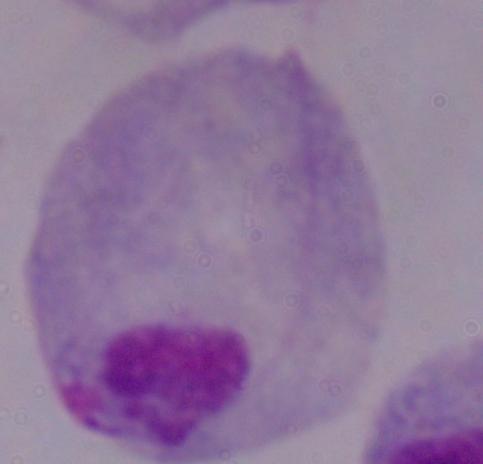

Summary:
  - Identification: trichomonad
  - Modality: micrograph
  - Magnification: 1000x